State which parasite is depicted.
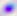
Toxoplasma gondii.

Summary:
  - Modality: photomicrograph
  - Magnification: 400x